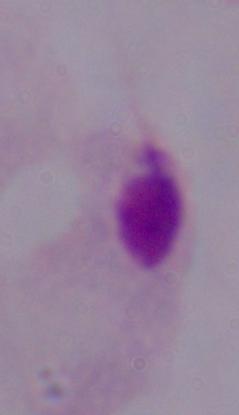
1000x magnification. Micrograph. A trichomonad is seen.